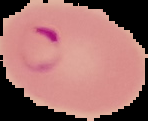

From a thin blood film. Malaria status: parasitized. Cell region segmented out of the field of view; the surrounding area is masked to black. Image is 148×121 pixels.